State which parasite is depicted.
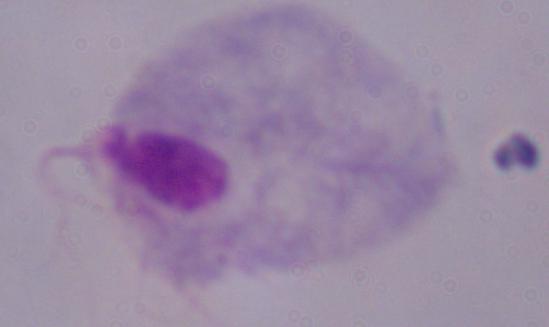

A trichomonad.

magnification: 1000x
modality: micrograph